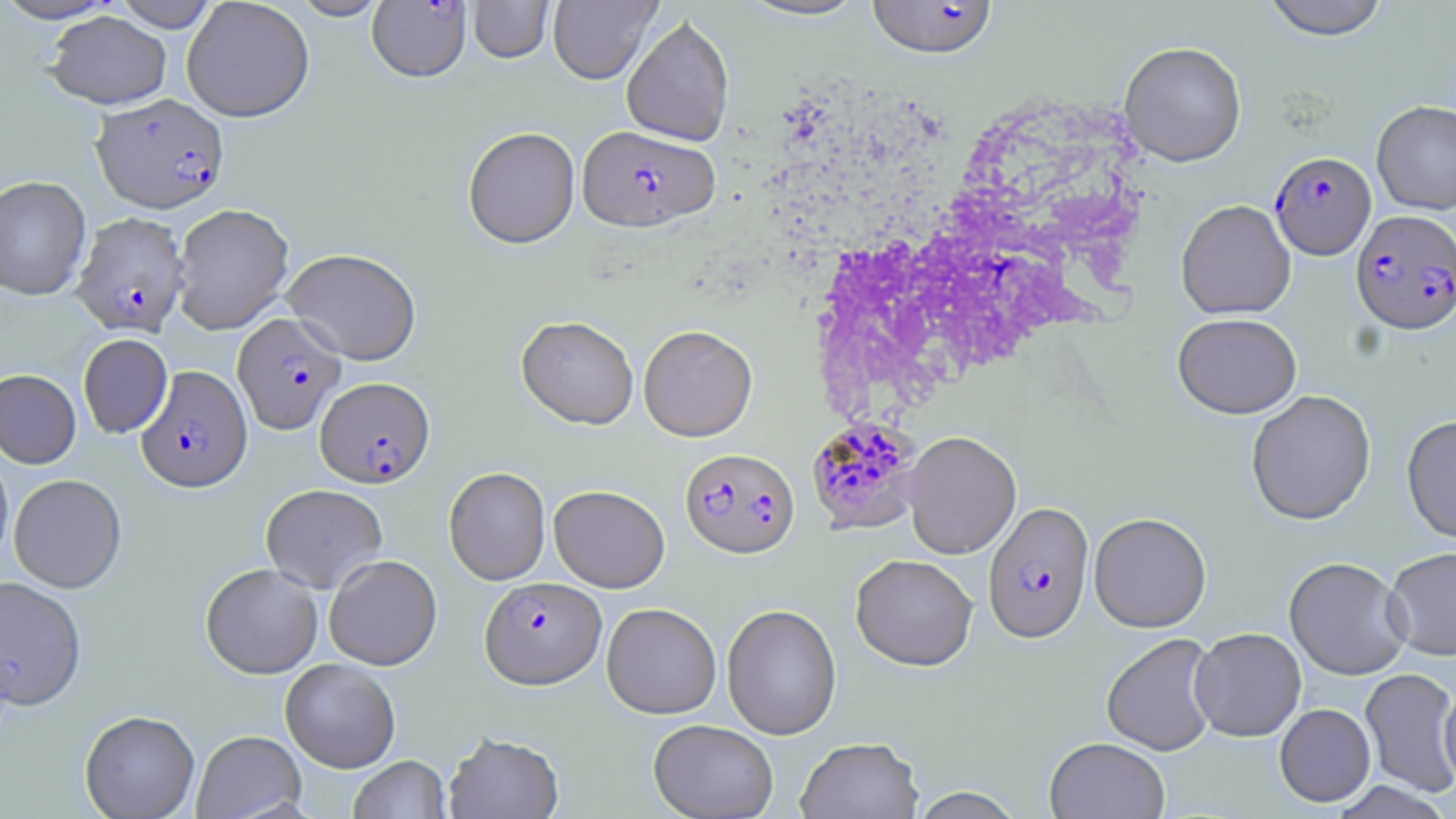

{
  "slide_level_diagnosis": "Plasmodium falciparum",
  "stain": "May-Grünwald-Giemsa",
  "uninfected_red_blood_cell_locations": "approximate bounding boxes as [x1, y1, x2, y2] in pixels: [0, 0, 123, 24], [181, 0, 315, 123], [290, 0, 389, 21], [548, 0, 661, 85], [737, 0, 871, 22], [1262, 0, 1390, 40], [111, 1, 221, 32], [468, 1, 554, 64], [45, 11, 172, 109], [621, 15, 735, 147], [1119, 41, 1247, 166], [1372, 100, 1456, 215], [462, 128, 580, 250], [0, 175, 91, 300], [1176, 199, 1296, 319], [171, 203, 294, 335], [281, 248, 422, 365], [1172, 312, 1301, 418], [516, 316, 638, 431], [638, 324, 758, 442], [78, 334, 172, 438], [0, 369, 81, 469], [1246, 389, 1376, 525], [1402, 414, 1456, 543], [902, 430, 1021, 559], [0, 448, 13, 571], [443, 467, 551, 585], [9, 474, 126, 593], [261, 484, 388, 593], [549, 484, 670, 592], [1089, 512, 1211, 632], [1384, 546, 1456, 660], [851, 554, 978, 670], [324, 555, 442, 670], [1284, 556, 1411, 680], [200, 564, 323, 679], [0, 576, 87, 710], [601, 602, 721, 719], [722, 603, 842, 739], [1190, 627, 1306, 741], [1101, 632, 1219, 756], [280, 659, 401, 773], [1360, 667, 1456, 797], [1439, 683, 1456, 791], [1274, 703, 1375, 806], [79, 710, 200, 819], [648, 719, 778, 819], [192, 730, 306, 819], [444, 731, 564, 818], [795, 736, 924, 819], [1045, 737, 1170, 819], [348, 756, 451, 818], [907, 787, 1025, 818]",
  "modality": "light microscopy",
  "plasmodium_falciparum_infected_red_blood_cell_locations": "approximate bounding boxes as [x1, y1, x2, y2] in pixels: [867, 0, 999, 60], [367, 1, 471, 85], [92, 94, 229, 214], [577, 126, 720, 233], [1270, 152, 1376, 260], [1351, 209, 1456, 335], [72, 213, 190, 337], [233, 312, 345, 434], [136, 366, 253, 494], [315, 376, 435, 488], [812, 420, 930, 537], [680, 447, 800, 559], [982, 501, 1094, 643], [480, 576, 606, 690]",
  "magnification": "1000x",
  "preparation": "thin blood smear",
  "field_of_view": "single",
  "image_size": "1456×819 pixels"
}